Locate leukocytes (white blood cells).
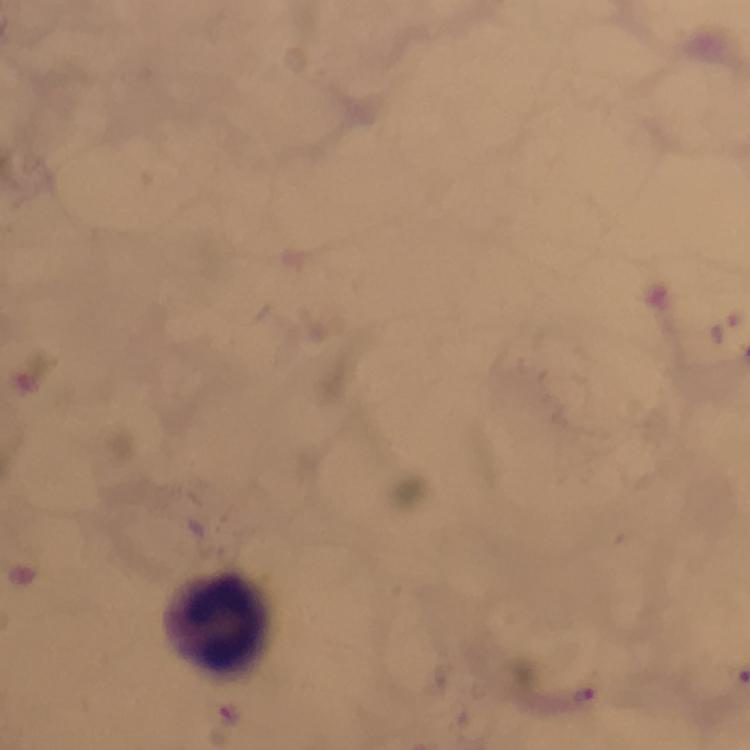

Approximate centers as (x, y) in pixels.
Leukocytes: (218, 621).

Plasmodium parasite locations: (587, 697). 100x magnification. Thick smear. A crop from one field of view. Giemsa-stained preparation. From a diagnostic examination for malaria. Image is 750×750 pixels. Immersion oil applied. Photographed through the microscope with a smartphone camera.